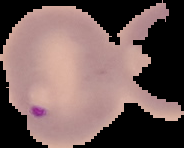

Image is 184×148 pixels. Malaria status: parasitized. The area outside the segmented cell region is set to black. From a thin blood film.